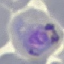

Summary:
  - Result: malaria parasites detected
  - Capture: smartphone camera at the microscope eyepiece
  - Image type: automatically extracted cell patch, resized to 64 × 64 pixels
  - Stain: Giemsa
  - Preparation: thin smear